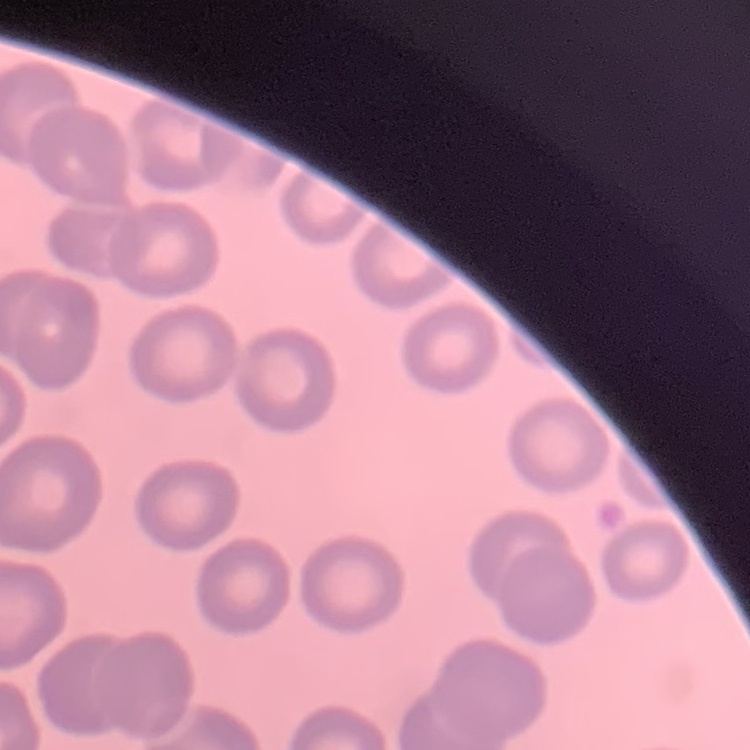

Summary:
  - Erythrocyte morphology: no rouleaux formation
  - Stain: Field's or Giemsa
  - Preparation: thin peripheral smear
  - Image type: one tile cut from a larger photomicrograph